Locate every Plasmodium ovale-infected red blood cell.
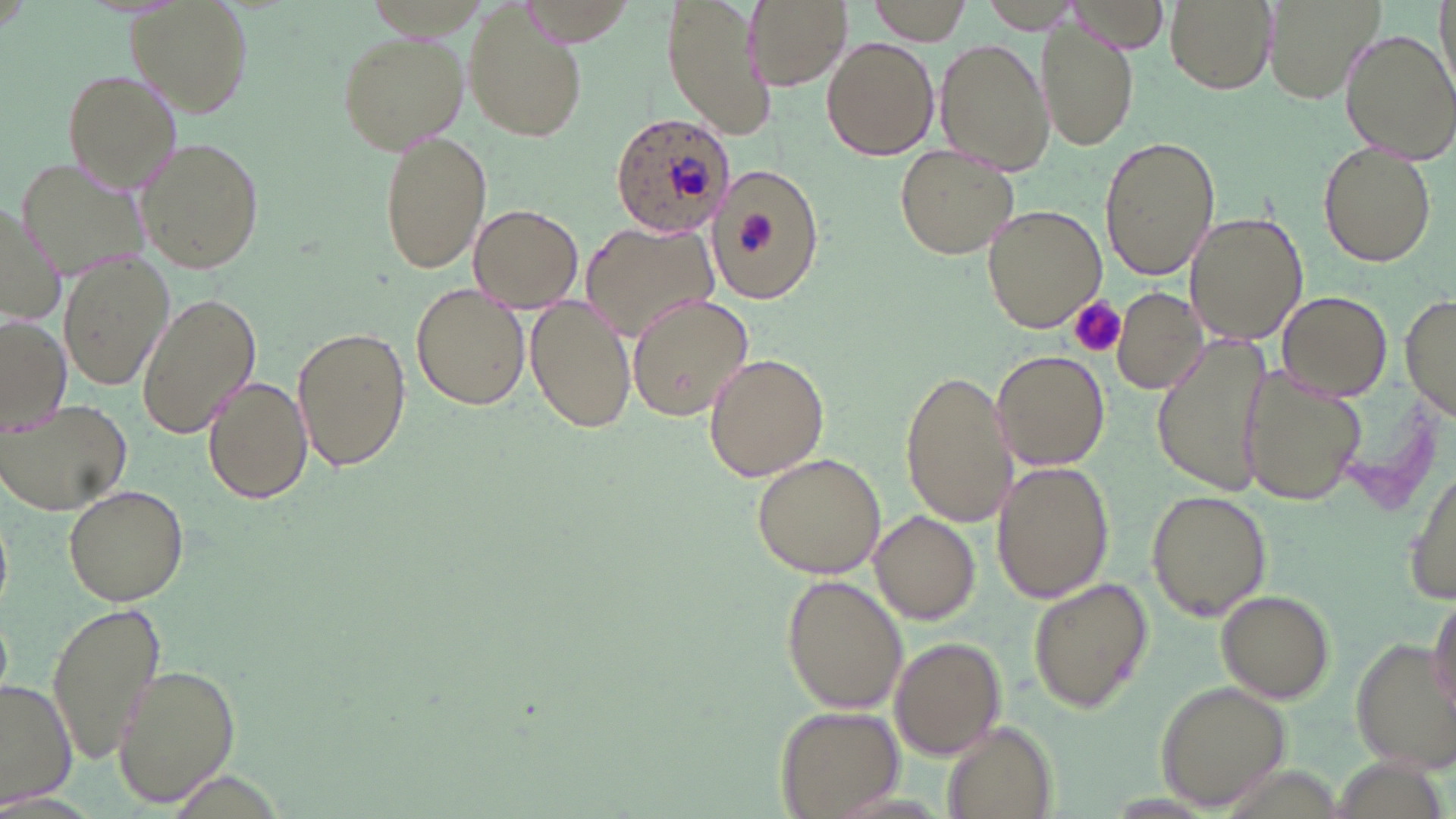
Approximate bounding boxes as (x1, y1, x2, y2) in pixels.
Plasmodium ovale-infected red blood cells: (609, 112, 737, 235).

slide_level_diagnosis: Plasmodium ovale
preparation: thin blood film
magnification: 1000x
image_size: 1456×819 pixels
modality: light microscopy
field_of_view: single
platelet_locations: 'approximate bounding boxes as (x1, y1, x2, y2) in pixels: (735, 211, 774, 258), (1069, 298, 1127, 359)'
stain: May-Grünwald-Giemsa
uninfected_red_blood_cell_locations: 'approximate bounding boxes as (x1, y1, x2, y2) in pixels: (130, 0, 253, 114), (663, 0, 774, 139), (745, 0, 851, 92), (869, 0, 976, 45), (983, 0, 1076, 33), (1165, 0, 1276, 94), (1264, 0, 1384, 104), (1433, 0, 1456, 100), (515, 1, 640, 47), (462, 5, 589, 143), (1037, 18, 1137, 153), (1339, 28, 1456, 164), (337, 29, 468, 153), (822, 36, 939, 161), (934, 38, 1054, 178), (62, 68, 183, 195), (378, 131, 491, 274), (1099, 134, 1219, 282), (131, 135, 266, 273), (1318, 143, 1437, 267), (891, 144, 1020, 261), (17, 156, 151, 276), (708, 166, 824, 300), (0, 200, 62, 328), (467, 204, 584, 312), (981, 204, 1106, 332), (1187, 211, 1309, 344), (581, 223, 717, 339), (58, 253, 173, 390), (411, 283, 529, 412), (1111, 288, 1206, 394), (1402, 289, 1455, 424), (1278, 290, 1393, 399), (136, 292, 262, 439), (524, 292, 635, 434), (625, 295, 754, 422), (1, 315, 72, 431), (292, 323, 413, 474), (1150, 331, 1279, 498), (992, 349, 1111, 471), (703, 352, 831, 482), (1240, 365, 1367, 507), (900, 367, 1018, 529), (202, 375, 314, 504), (1, 398, 132, 515), (750, 452, 886, 579), (1407, 457, 1456, 607), (992, 459, 1114, 602), (62, 482, 190, 607), (1146, 488, 1272, 620), (869, 510, 980, 624), (783, 574, 909, 713), (1028, 575, 1153, 714), (1215, 591, 1335, 704), (1428, 593, 1455, 718), (46, 598, 166, 767), (889, 635, 1008, 760), (1346, 638, 1454, 770), (112, 660, 242, 808), (0, 680, 76, 806), (1156, 682, 1291, 809), (776, 705, 903, 818), (940, 722, 1058, 819)'